Assess this cell for malaria.
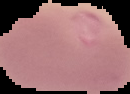

It is uninfected.

Summary:
  - Image size: 130×94 pixels
  - Preparation: thin blood smear
  - Image type: segmented cell region with the area outside set to black